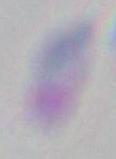

identification = Toxoplasma gondii
magnification = 1000x
modality = photomicrograph